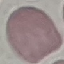
Result: no malaria parasites seen. Cell patch, automatically extracted from a larger field of view and resized to 64 × 64 pixels. Acquired by smartphone through the microscope eyepiece. Giemsa-stained preparation. Thin blood film.